Name the parasite shown.
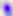

This is Toxoplasma gondii.

modality = micrograph
magnification = 400x